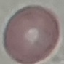
result = no malaria parasites seen
preparation = thin smear
image type = automatically extracted cell patch, resized to 64 × 64 pixels
capture = smartphone camera at the microscope eyepiece
stain = Giemsa